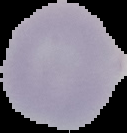
Summary:
  - Result: no Plasmodium parasites detected
  - Image type: segmented cell region with the area outside set to black
  - Image size: 127×133 pixels
  - Preparation: thin blood smear